Report the malaria status of this cell.
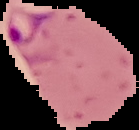
Parasitized.

image size = 139×130 pixels
preparation = thin blood film
image type = segmented cell region with the area outside set to black